State which parasite is depicted.
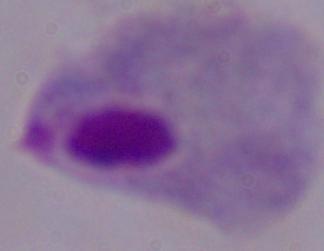
This is a trichomonad.

modality = photomicrograph
magnification = 1000x